Describe the morphology of the erythrocytes.
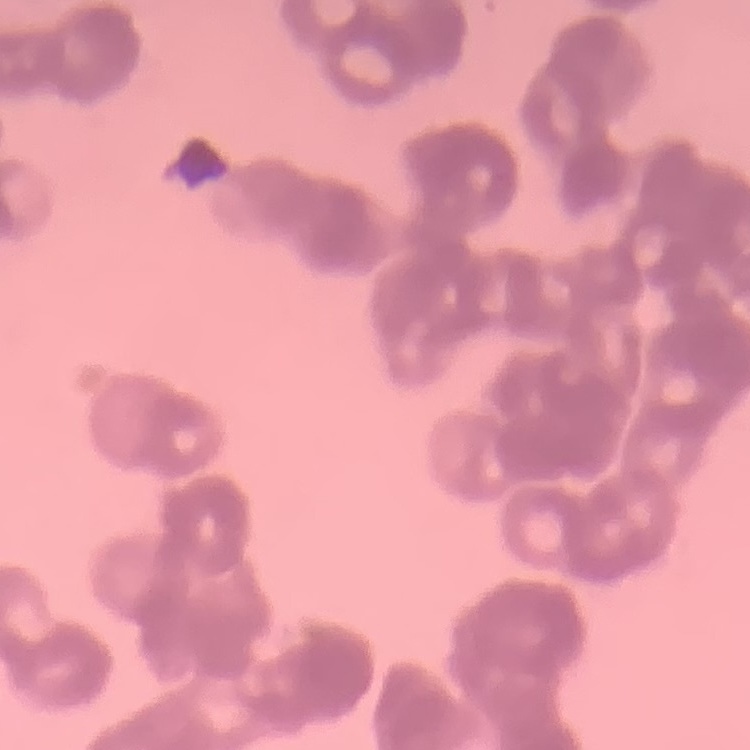

Rouleaux formation.

Thin blood smear. Stained with either Field's or Giemsa. Square crop of a larger photomicrograph.